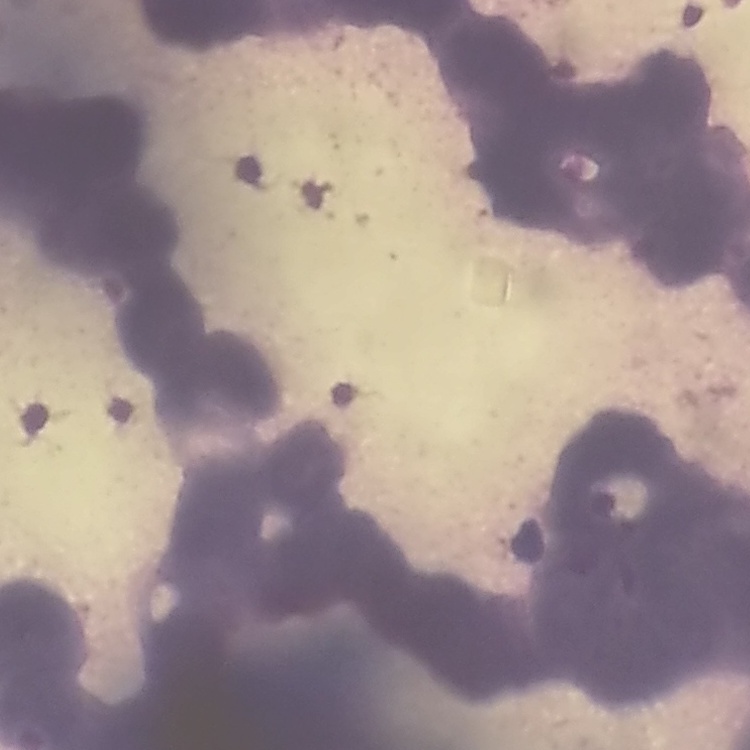
red blood cell morphology = rouleaux formation
stain = Field's or Giemsa
preparation = thin peripheral smear
image type = square crop of a larger photomicrograph